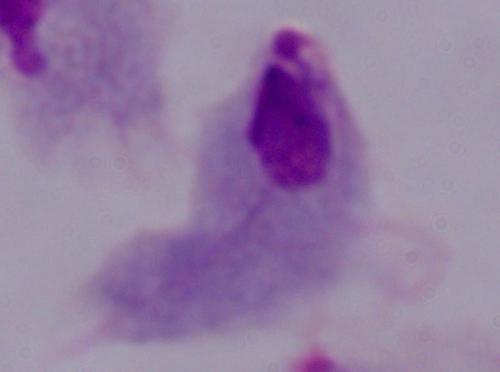

Summary:
  - Magnification: 1000x
  - Modality: micrograph
  - Identification: trichomonad